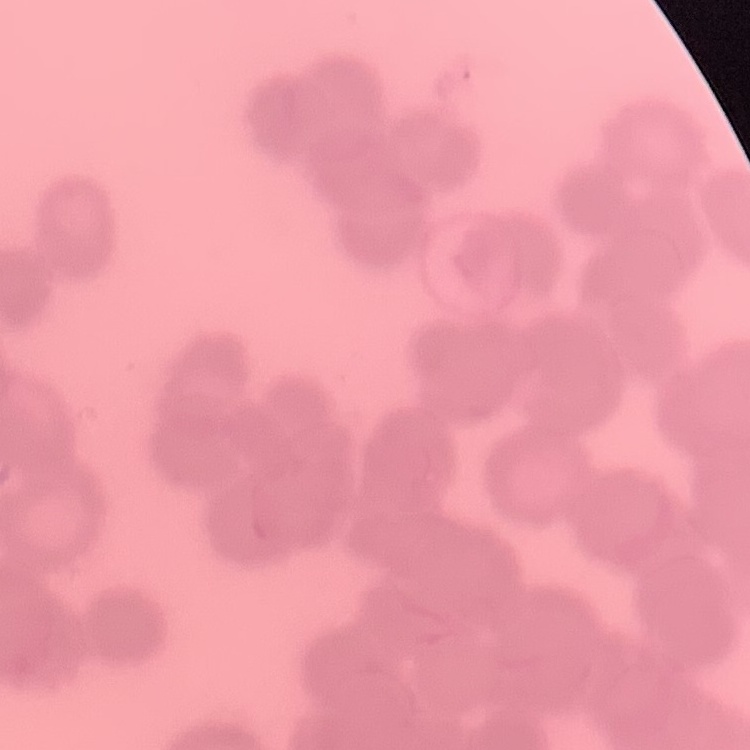 The erythrocytes exhibit rouleaux formation. Square crop of a larger photomicrograph. Thin blood film. Stained with either Field's or Giemsa.